Classify this cell by malaria status.
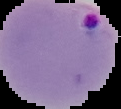
It is parasitized.

From a thin blood film. Image is 121×109 pixels. Cell region segmented out of the field of view; the surrounding area is masked to black.